Name the cell type shown.
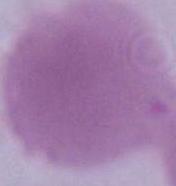

This is an erythrocyte.

Summary:
  - Magnification: 1000x
  - Modality: micrograph